Outline each Plasmodium malariae-infected red blood cell.
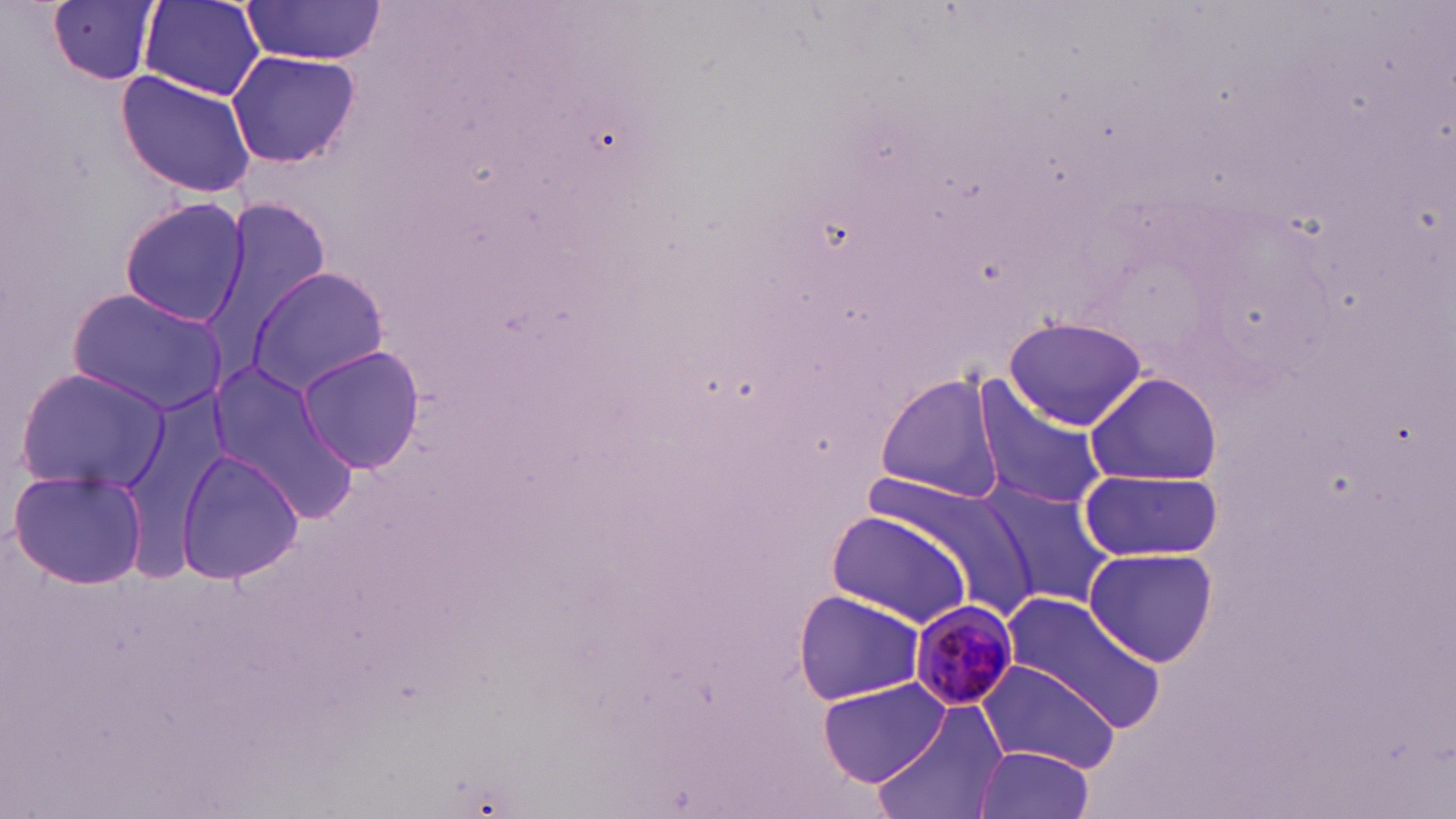
Approximate bounding boxes as named x1/y1/x2/y2 corners in pixels.
Plasmodium malariae-infected red blood cells: (x1=908, y1=599, x2=1019, y2=710).

Summary:
  - Uninfected red blood cell locations: (x1=49, y1=0, x2=161, y2=85), (x1=141, y1=0, x2=266, y2=100), (x1=240, y1=4, x2=381, y2=66), (x1=226, y1=50, x2=360, y2=169), (x1=116, y1=70, x2=259, y2=201), (x1=118, y1=195, x2=249, y2=328), (x1=203, y1=201, x2=332, y2=371), (x1=246, y1=266, x2=391, y2=394), (x1=67, y1=287, x2=229, y2=417), (x1=1002, y1=316, x2=1148, y2=429), (x1=295, y1=344, x2=426, y2=476), (x1=204, y1=358, x2=359, y2=519), (x1=14, y1=367, x2=172, y2=494), (x1=1086, y1=370, x2=1221, y2=487), (x1=874, y1=374, x2=1003, y2=500), (x1=969, y1=376, x2=1108, y2=514), (x1=173, y1=445, x2=302, y2=590), (x1=1076, y1=466, x2=1223, y2=563), (x1=9, y1=467, x2=151, y2=591), (x1=976, y1=478, x2=1115, y2=609), (x1=824, y1=509, x2=975, y2=626), (x1=1082, y1=545, x2=1217, y2=669), (x1=1000, y1=589, x2=1169, y2=732), (x1=792, y1=590, x2=928, y2=705), (x1=975, y1=658, x2=1123, y2=772), (x1=815, y1=678, x2=949, y2=786), (x1=873, y1=703, x2=1010, y2=819), (x1=974, y1=746, x2=1096, y2=819)
  - Slide-level diagnosis: Plasmodium malariae
  - Field of view: single
  - Image size: 1456×819 pixels
  - Stain: May-Grünwald-Giemsa
  - Magnification: 1000x
  - Modality: optical microscopy
  - Preparation: thin blood film